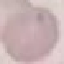
Malaria status: uninfected. Photographed with a smartphone camera at the microscope eyepiece. Automatically extracted cell patch, resized to 64 × 64 pixels. Thin blood smear. Giemsa-stained preparation.